State the blood parasite species.
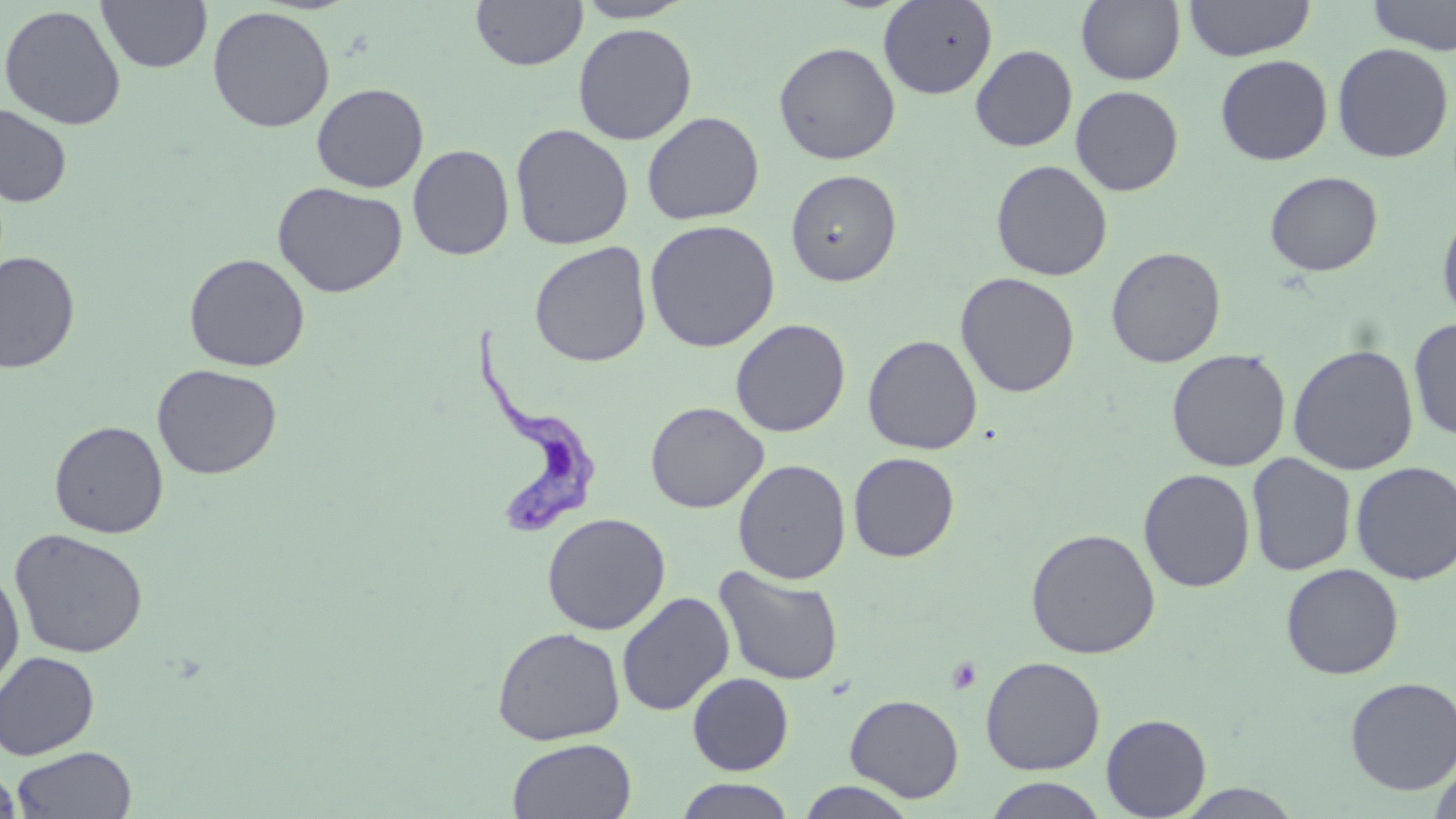
Trypanosoma brucei.

image_size: 1456×819 pixels
trypanosoma_brucei_locations: 'approximate bounding boxes as [x1, y1, x2, y2] in pixels: [468, 322, 602, 537]'
modality: light microscopy
stain: May-Grünwald-Giemsa
field_of_view: single
magnification: 1000x
preparation: thin blood film
uninfected_red_blood_cell_locations: 'approximate bounding boxes as [x1, y1, x2, y2] in pixels: [96, 0, 213, 74], [470, 0, 588, 71], [572, 0, 697, 23], [878, 0, 998, 100], [1076, 0, 1185, 85], [1183, 0, 1315, 62], [1364, 0, 1456, 56], [0, 4, 126, 130], [207, 5, 335, 133], [573, 22, 697, 145], [773, 41, 901, 165], [1332, 42, 1454, 163], [970, 44, 1077, 151], [1215, 54, 1333, 165], [311, 83, 429, 193], [1070, 85, 1184, 196], [0, 104, 72, 207], [641, 111, 764, 225], [509, 123, 634, 250], [407, 144, 515, 261], [990, 159, 1113, 282], [785, 169, 902, 287], [1265, 171, 1383, 276], [272, 181, 407, 298], [1436, 204, 1456, 327], [644, 219, 780, 352], [529, 241, 653, 367], [1105, 246, 1226, 368], [0, 251, 80, 373], [183, 252, 310, 372], [956, 271, 1080, 398], [1408, 317, 1456, 441], [730, 318, 851, 438], [862, 334, 982, 455], [1288, 344, 1419, 475], [1166, 348, 1291, 472], [152, 363, 282, 480], [645, 401, 768, 514], [48, 420, 169, 539], [848, 452, 960, 561], [1246, 453, 1356, 577], [733, 459, 851, 584], [1350, 461, 1456, 585], [1138, 468, 1255, 592], [541, 512, 671, 635], [9, 528, 149, 659], [1025, 528, 1161, 659], [1280, 563, 1404, 680], [713, 565, 845, 686], [0, 566, 25, 696], [616, 591, 735, 717], [491, 626, 625, 745], [0, 650, 99, 759], [980, 656, 1106, 775], [687, 672, 794, 776], [1345, 676, 1456, 795], [845, 694, 964, 803], [1101, 713, 1212, 818], [507, 738, 637, 819], [12, 746, 136, 818], [1428, 759, 1456, 819], [0, 765, 21, 817], [984, 776, 1108, 818], [674, 778, 796, 818], [795, 781, 918, 819], [1174, 784, 1304, 818]'
platelet_locations: 'approximate bounding boxes as [x1, y1, x2, y2] in pixels: [947, 657, 982, 695]'